Give a bounding box for every malaria parasite.
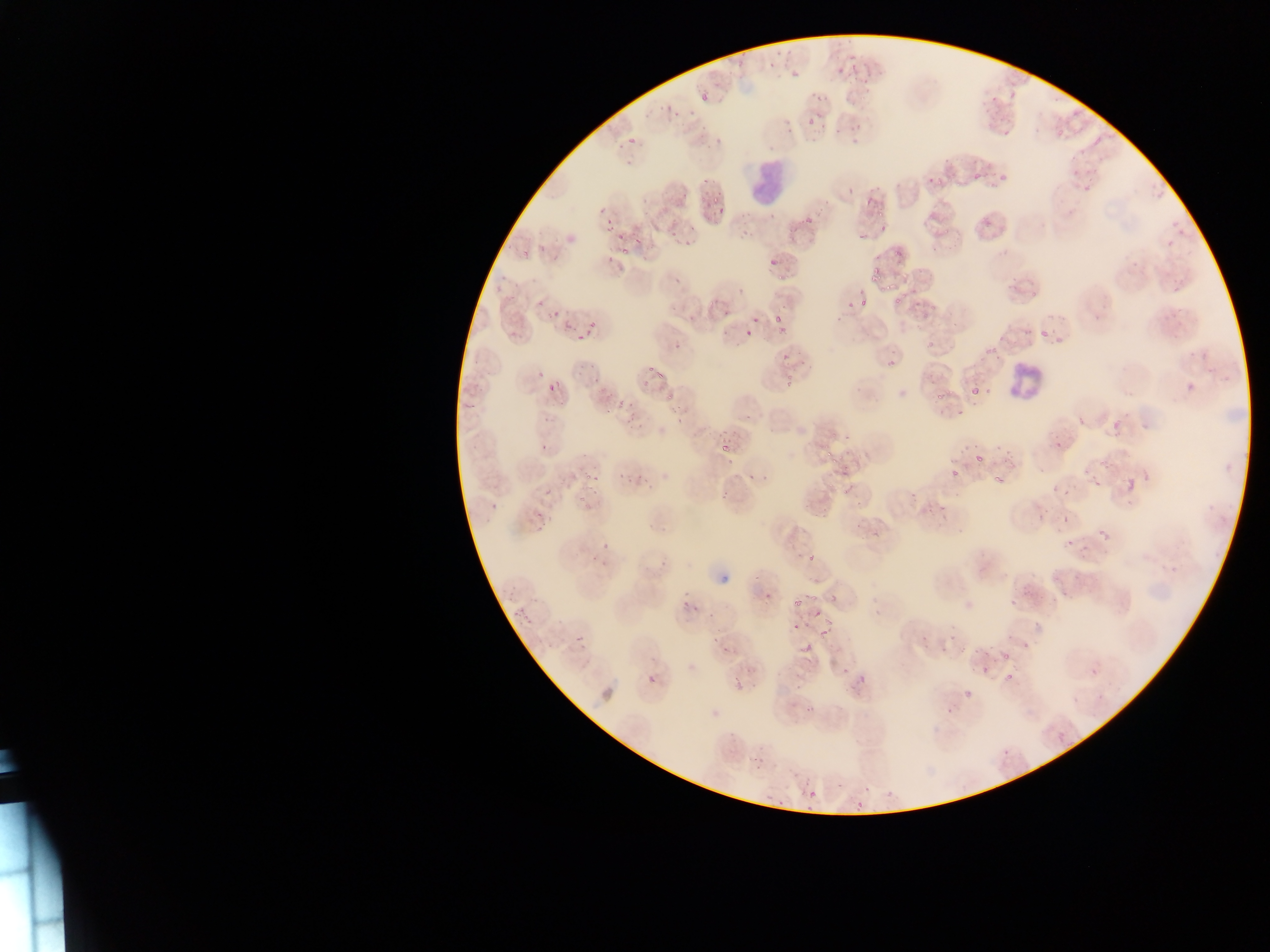

Approximate bounding boxes as [left, top, right, bottom] in pixels.
Malaria parasites: [763, 44, 790, 69], [729, 48, 749, 69], [822, 48, 847, 66], [839, 65, 866, 84], [786, 67, 804, 79], [711, 77, 732, 94], [1006, 82, 1023, 105], [984, 93, 1001, 112], [695, 95, 710, 107], [646, 102, 670, 117], [666, 109, 684, 123], [806, 116, 817, 127], [997, 120, 1013, 143], [847, 124, 862, 146], [703, 126, 726, 147], [628, 136, 636, 144], [1095, 137, 1102, 145], [613, 144, 626, 155], [992, 167, 1008, 182], [926, 169, 946, 184], [973, 173, 981, 181], [702, 177, 710, 185], [860, 192, 877, 207], [704, 193, 722, 212], [594, 201, 608, 218], [795, 212, 816, 224], [977, 215, 993, 229], [877, 217, 897, 232], [1170, 218, 1180, 229], [603, 219, 614, 231], [850, 226, 866, 244], [1178, 227, 1192, 237], [616, 231, 628, 242], [683, 231, 701, 249], [668, 233, 678, 247], [1164, 238, 1174, 246], [890, 242, 900, 262], [519, 243, 533, 264], [620, 248, 632, 260], [604, 251, 615, 268], [768, 258, 781, 269], [863, 268, 881, 285], [1170, 275, 1186, 296], [882, 290, 906, 312], [531, 293, 549, 308], [858, 297, 869, 306], [711, 303, 732, 323], [548, 304, 570, 327], [770, 313, 784, 324], [750, 317, 760, 323], [570, 321, 596, 338], [772, 328, 785, 341], [1040, 330, 1049, 340], [1053, 332, 1065, 350], [739, 333, 752, 342], [671, 342, 681, 350], [981, 344, 997, 359], [775, 345, 797, 362], [525, 359, 548, 387], [882, 360, 896, 370], [643, 365, 662, 381], [592, 371, 606, 383], [779, 374, 796, 391], [1186, 380, 1196, 398], [547, 382, 559, 393], [970, 387, 980, 396], [935, 390, 948, 401], [663, 392, 676, 404], [605, 401, 625, 413], [1076, 405, 1088, 435], [625, 407, 648, 434], [667, 407, 686, 421], [1103, 414, 1125, 439], [714, 425, 743, 453], [537, 438, 556, 454], [1052, 438, 1064, 452], [822, 439, 844, 470], [970, 451, 989, 468], [990, 463, 1009, 485], [947, 467, 959, 482], [620, 470, 650, 487], [747, 470, 760, 481], [586, 472, 598, 483], [1123, 477, 1137, 494], [1092, 478, 1102, 488], [1048, 485, 1071, 494], [543, 487, 557, 497], [716, 491, 731, 505], [576, 496, 594, 512], [1031, 503, 1051, 520], [530, 508, 546, 530], [1059, 511, 1071, 526], [1097, 527, 1109, 544], [1062, 536, 1072, 552], [597, 539, 611, 550], [1077, 541, 1094, 566], [588, 553, 602, 567], [808, 554, 817, 563], [1056, 588, 1072, 599], [826, 590, 841, 606], [789, 591, 804, 615], [681, 596, 700, 609], [1008, 596, 1019, 611], [515, 608, 526, 619], [807, 611, 827, 618], [792, 618, 803, 632], [819, 621, 836, 641], [950, 621, 957, 641], [712, 630, 726, 646], [573, 633, 585, 645], [802, 634, 816, 653], [1020, 642, 1031, 653], [723, 644, 736, 667], [938, 644, 947, 660], [958, 645, 966, 653], [994, 648, 1010, 665], [980, 661, 991, 675], [834, 664, 850, 677], [731, 665, 758, 689], [856, 665, 871, 684], [1090, 667, 1098, 677], [647, 673, 658, 684], [794, 673, 810, 691], [1000, 673, 1018, 687], [952, 690, 982, 701], [803, 700, 821, 714], [941, 705, 953, 717], [1058, 734, 1066, 743], [751, 743, 765, 774], [1000, 745, 1011, 757], [862, 782, 870, 792], [808, 790, 817, 799], [882, 792, 896, 806], [776, 799, 785, 807], [855, 801, 862, 809], [802, 803, 815, 813].

Leukocyte locations: [738, 152, 789, 203], [1002, 357, 1042, 405]. Thin blood film. Image is 1270×952 pixels. Single field of view. Collected in Ghana. Mobile-phone photograph taken through the microscope.